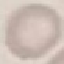

result: no malaria parasites detected
preparation: thin smear
image_type: cell patch, automatically extracted from a larger field of view and resized to 64 × 64 pixels
capture: smartphone through the microscope eyepiece
stain: Giemsa